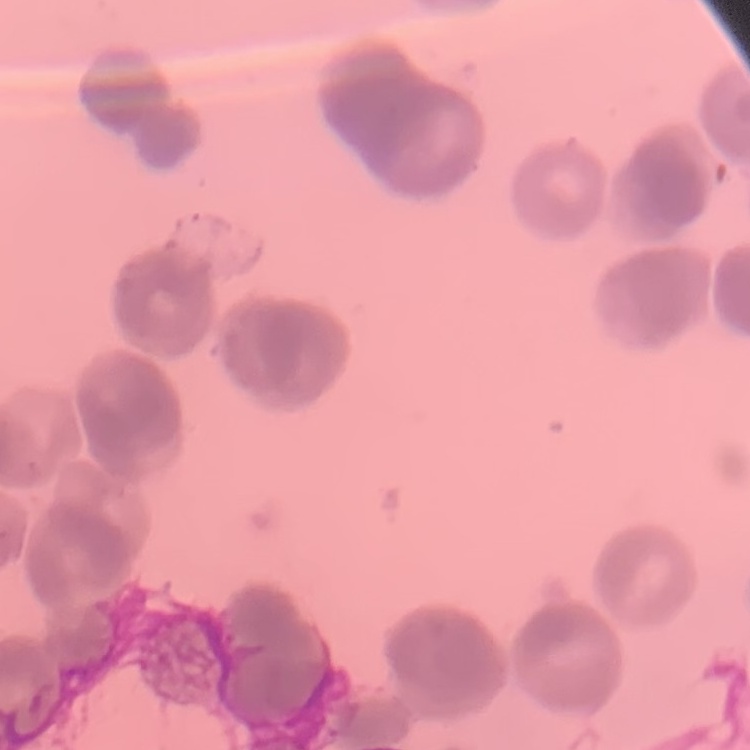 The red blood cells exhibit rouleaux formation. Thin blood film. Stained with either Field's or Giemsa. One tile cut from a larger photomicrograph.